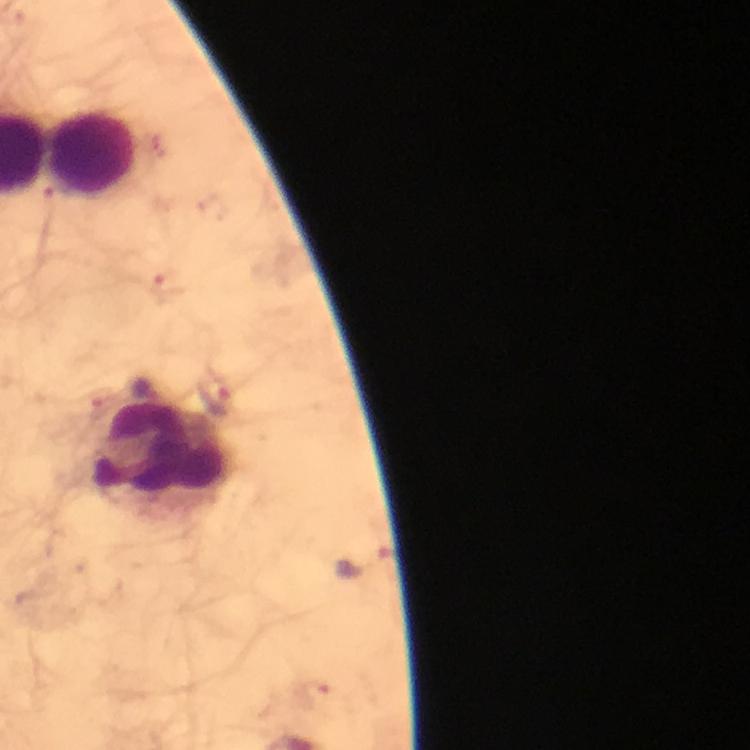

Approximate object centers, in pixels from the top-left corner. Leukocyte locations: (x=93, y=154), (x=160, y=453). Plasmodium parasite locations: (x=152, y=146), (x=60, y=197), (x=169, y=288), (x=217, y=399), (x=100, y=405), (x=363, y=562), (x=317, y=694). Immersion oil was used. Image is 750×750 pixels. At 100x magnification. From a malaria diagnostic workup. Thick smear. Giemsa-stained preparation. Photographed with a smartphone mounted on the microscope. A crop from one field of view.